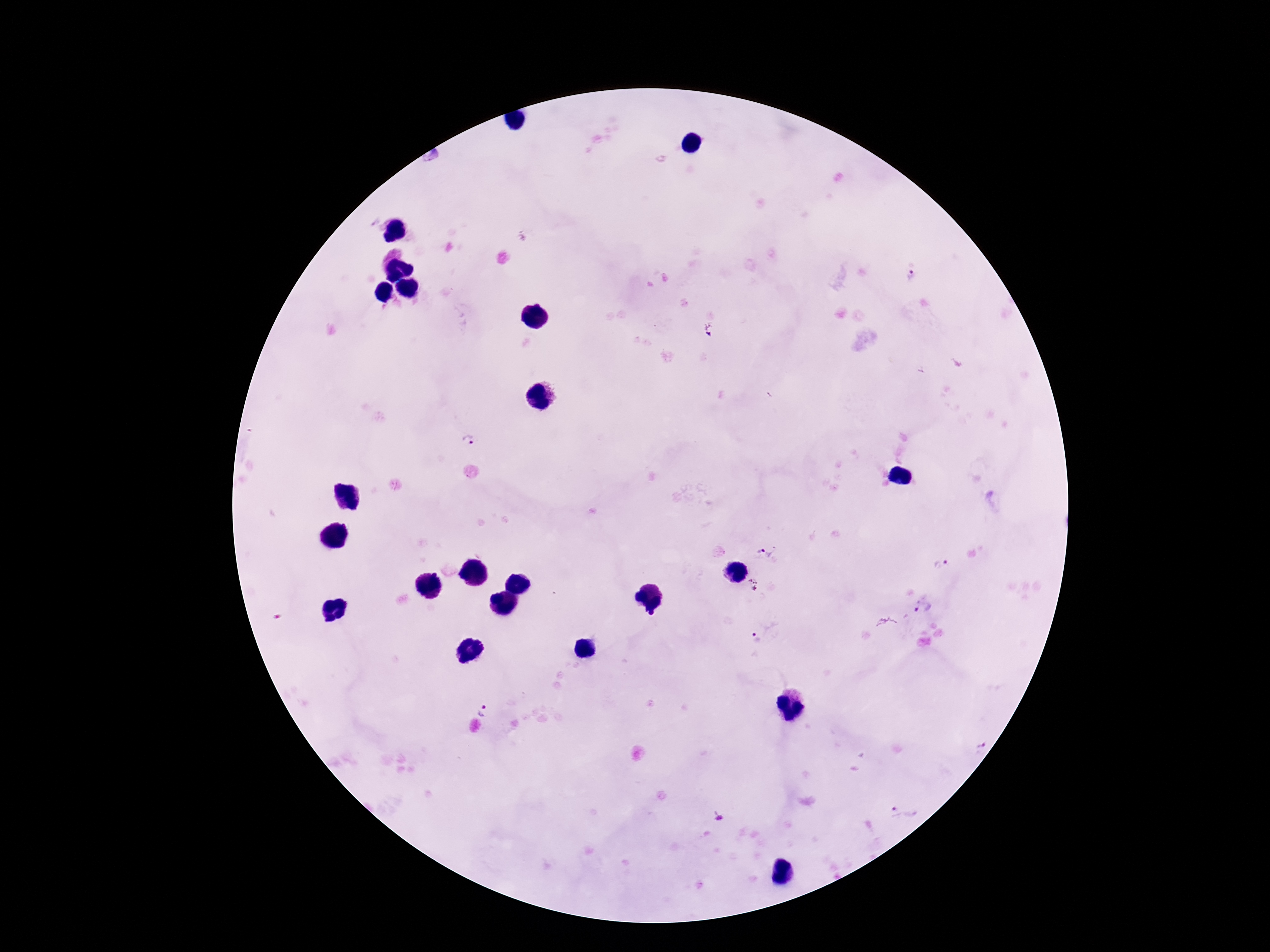

patient malaria status = positive
stain = Giemsa
magnification = 100x
capture = smartphone camera through the microscope eyepiece
preparation = thick blood smear
field of view = single
Plasmodium parasite locations = approximate centers as (x, y) in pixels: (912, 276), (711, 331), (468, 439), (764, 547), (941, 564), (753, 584), (923, 608), (755, 637), (483, 709), (981, 748), (903, 812)
image size = 1270×952 pixels